Outline each Plasmodium ovale-infected red blood cell.
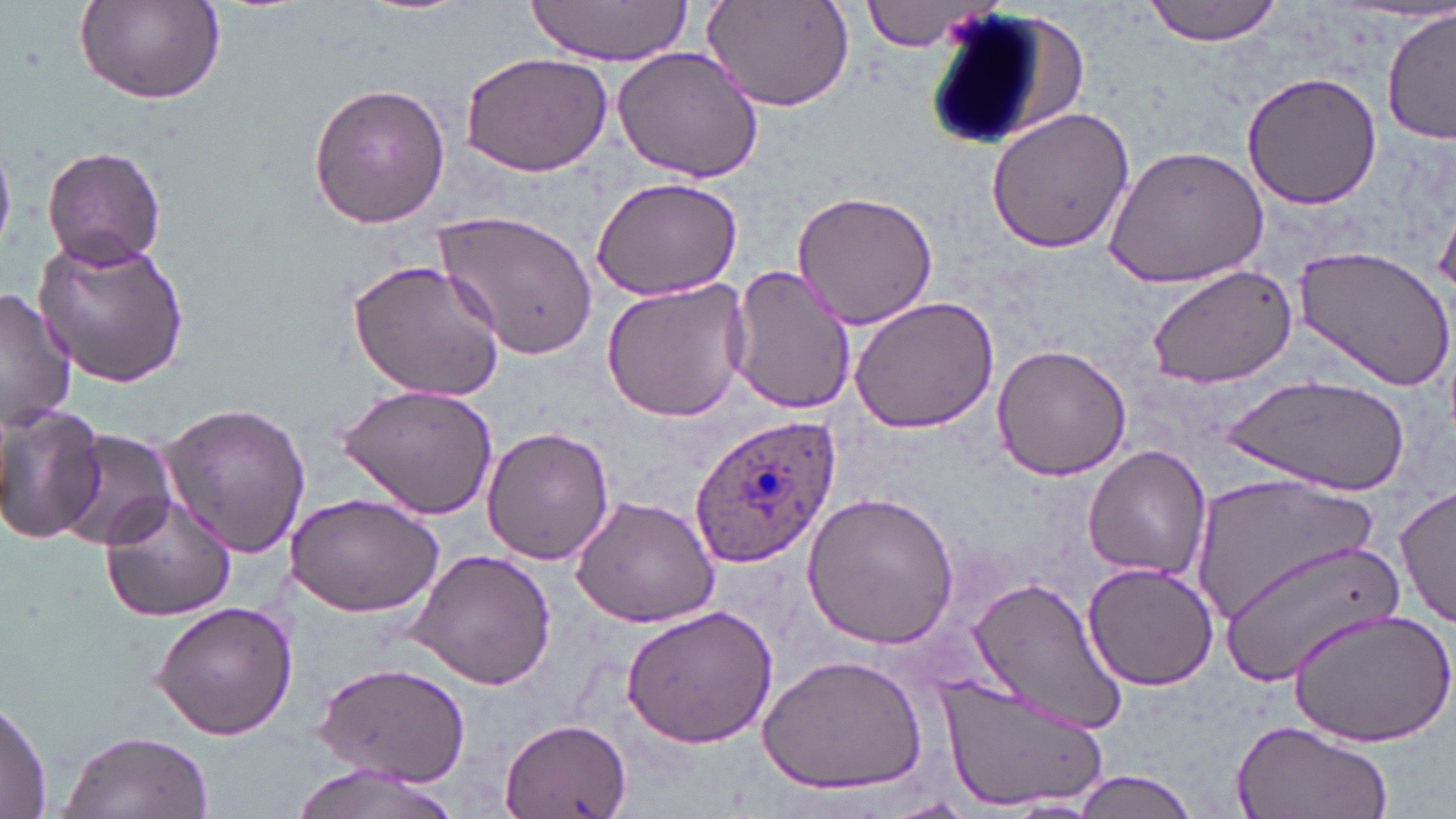
Approximate bounding boxes as named x1/y1/x2/y2 corners in pixels.
Plasmodium ovale-infected red blood cells: (x1=684, y1=412, x2=844, y2=569).

{
  "slide_level_diagnosis": "Plasmodium ovale",
  "field_of_view": "single",
  "stain": "May-Grünwald-Giemsa",
  "image_size": "1456×819 pixels",
  "magnification": "1000x",
  "modality": "optical microscopy",
  "preparation": "thin blood smear",
  "uninfected_red_blood_cell_locations": "approximate bounding boxes as named x1/y1/x2/y2 corners in pixels: (x1=73, y1=0, x2=226, y2=107), (x1=1141, y1=0, x2=1287, y2=45), (x1=525, y1=1, x2=695, y2=66), (x1=861, y1=1, x2=1001, y2=52), (x1=699, y1=2, x2=855, y2=113), (x1=917, y1=5, x2=1088, y2=155), (x1=1381, y1=8, x2=1455, y2=146), (x1=612, y1=46, x2=764, y2=184), (x1=458, y1=50, x2=615, y2=177), (x1=1243, y1=72, x2=1382, y2=211), (x1=307, y1=81, x2=452, y2=230), (x1=984, y1=105, x2=1137, y2=256), (x1=41, y1=145, x2=167, y2=269), (x1=1101, y1=146, x2=1267, y2=289), (x1=590, y1=175, x2=743, y2=300), (x1=791, y1=189, x2=942, y2=329), (x1=433, y1=211, x2=598, y2=360), (x1=33, y1=235, x2=192, y2=388), (x1=1292, y1=246, x2=1454, y2=394), (x1=345, y1=256, x2=507, y2=404), (x1=1146, y1=263, x2=1298, y2=388), (x1=727, y1=264, x2=856, y2=417), (x1=600, y1=278, x2=754, y2=421), (x1=0, y1=288, x2=77, y2=432), (x1=849, y1=295, x2=998, y2=434), (x1=992, y1=345, x2=1133, y2=481), (x1=1226, y1=376, x2=1411, y2=494), (x1=335, y1=383, x2=499, y2=519), (x1=157, y1=400, x2=311, y2=557), (x1=0, y1=403, x2=105, y2=545), (x1=481, y1=426, x2=615, y2=565), (x1=55, y1=430, x2=177, y2=552), (x1=1083, y1=445, x2=1213, y2=581), (x1=1194, y1=471, x2=1379, y2=628), (x1=1395, y1=484, x2=1456, y2=627), (x1=99, y1=491, x2=238, y2=621), (x1=801, y1=491, x2=960, y2=648), (x1=286, y1=492, x2=444, y2=617), (x1=570, y1=494, x2=722, y2=628), (x1=1219, y1=538, x2=1404, y2=684), (x1=408, y1=547, x2=557, y2=692), (x1=1083, y1=562, x2=1218, y2=689), (x1=965, y1=575, x2=1128, y2=737), (x1=150, y1=600, x2=298, y2=741), (x1=621, y1=603, x2=780, y2=749), (x1=1287, y1=609, x2=1455, y2=748), (x1=758, y1=653, x2=928, y2=796), (x1=310, y1=660, x2=471, y2=787), (x1=938, y1=674, x2=1111, y2=814), (x1=0, y1=697, x2=52, y2=815), (x1=500, y1=716, x2=635, y2=819), (x1=1231, y1=720, x2=1393, y2=819), (x1=58, y1=728, x2=214, y2=819), (x1=286, y1=764, x2=465, y2=819), (x1=1071, y1=769, x2=1201, y2=819), (x1=874, y1=798, x2=982, y2=819)"
}